Name the parasite shown.
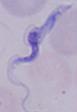

A trypanosome.

Summary:
  - Modality: micrograph
  - Magnification: 1000x